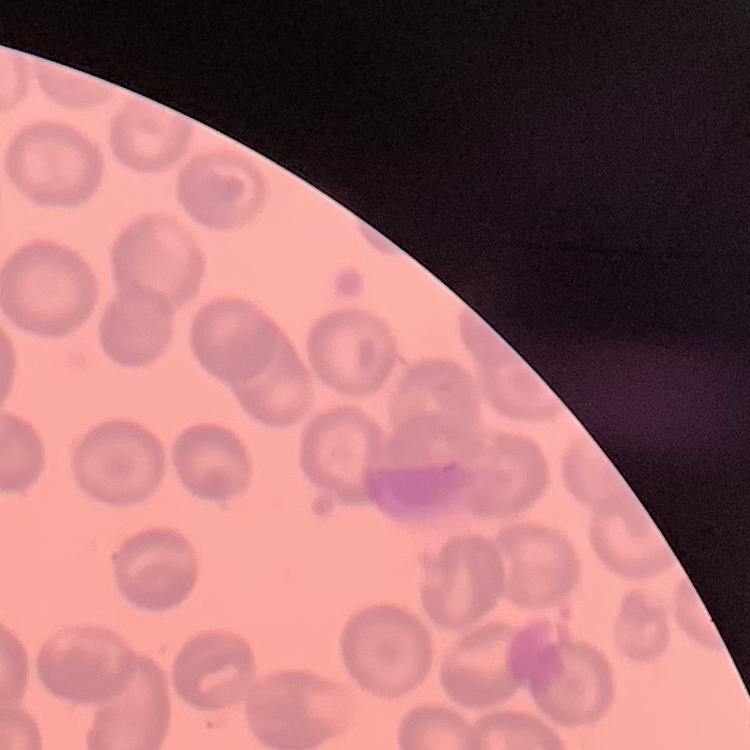
Summary:
  - Erythrocyte morphology: no rouleaux formation
  - Stain: Field's or Giemsa
  - Image type: square crop of a larger photomicrograph
  - Preparation: thin blood film